Give the position of every malaria parasite.
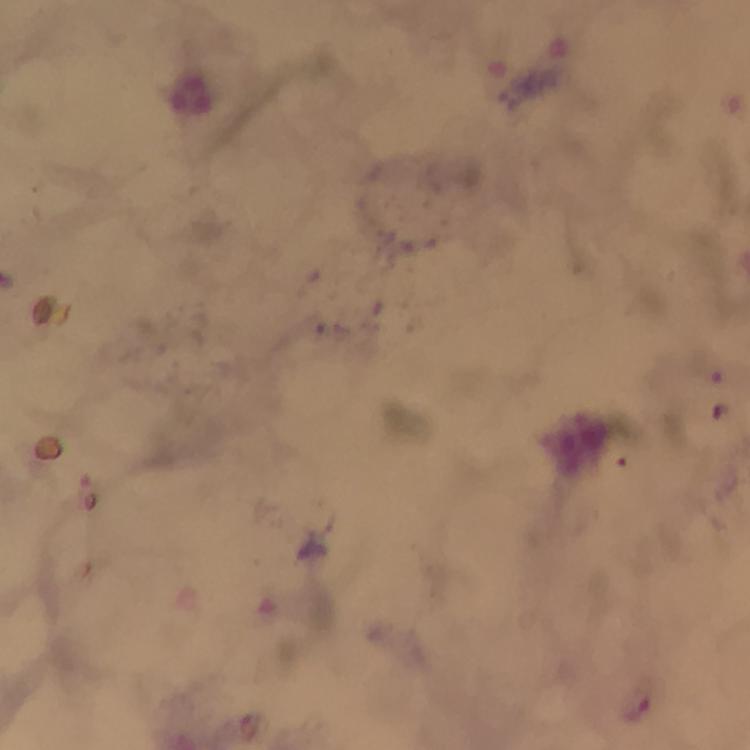
Approximate centers as (x, y) in pixels.
Malaria parasites: (640, 708).

From a diagnostic examination for malaria. Thick blood smear. Image is 750×750 pixels. Giemsa stain. Cropped region of a single field of view. Photographed through the microscope with a smartphone camera. Immersion oil applied. At 100x magnification.